State the blood parasite species.
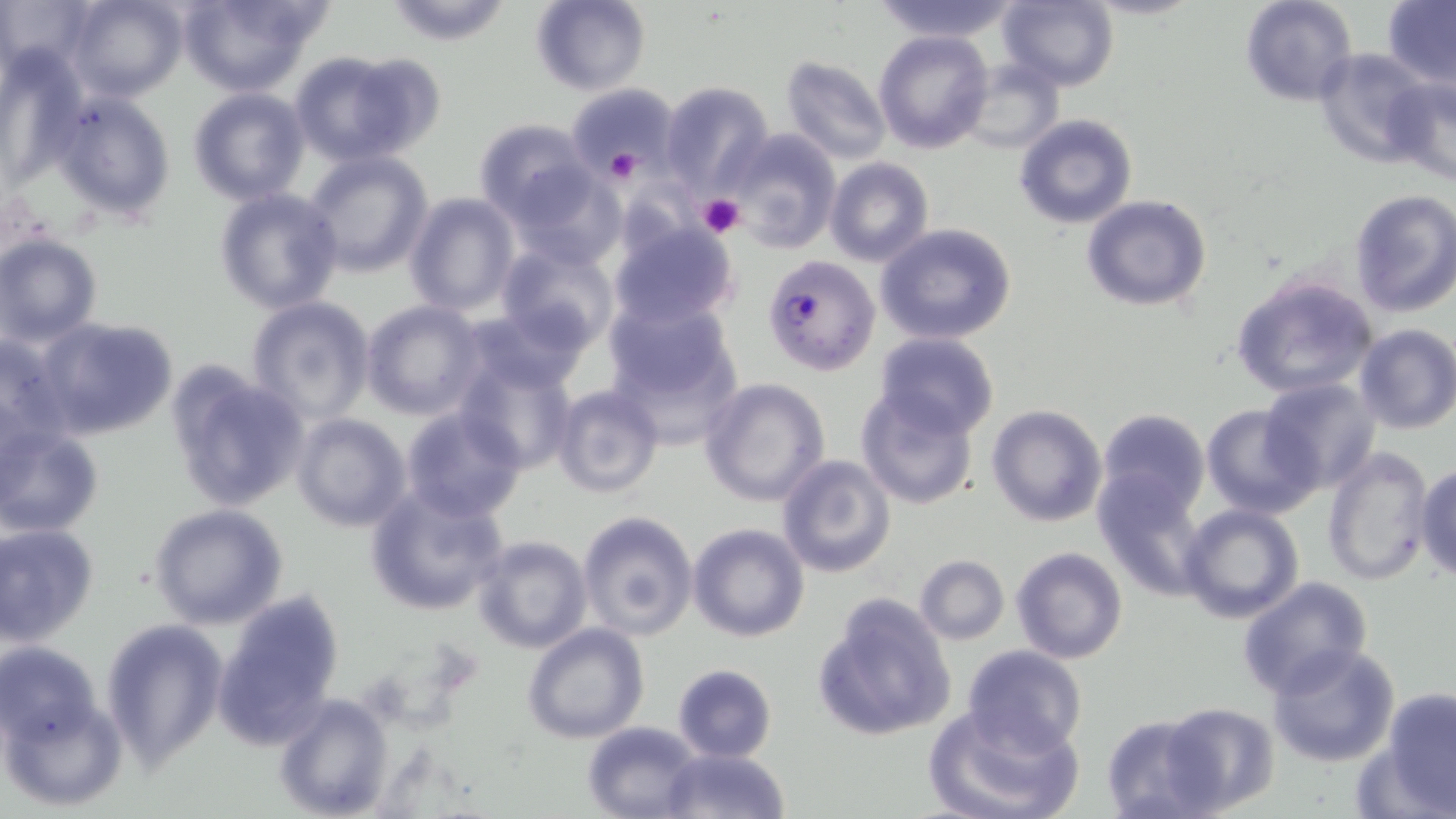
Plasmodium falciparum.

modality = optical microscopy
platelet locations = approximate bounding boxes as [x1, y1, x2, y2] in pixels: [606, 149, 642, 183], [697, 193, 747, 238]
image size = 1456×819 pixels
uninfected red blood cell locations = approximate bounding boxes as [x1, y1, x2, y2] in pixels: [0, 0, 93, 82], [65, 0, 188, 102], [383, 0, 516, 46], [870, 0, 1021, 42], [998, 0, 1119, 91], [1239, 0, 1358, 106], [531, 1, 652, 95], [1380, 1, 1456, 86], [172, 2, 328, 93], [874, 30, 994, 154], [1314, 47, 1435, 166], [287, 51, 428, 164], [778, 55, 892, 165], [959, 60, 1062, 154], [1383, 74, 1456, 188], [565, 82, 682, 178], [661, 82, 775, 198], [187, 87, 310, 205], [52, 91, 176, 223], [1014, 114, 1138, 230], [474, 120, 594, 225], [723, 128, 840, 253], [303, 149, 434, 278], [825, 159, 933, 267], [510, 164, 626, 267], [214, 188, 344, 314], [1349, 189, 1456, 317], [403, 191, 520, 316], [1083, 195, 1211, 311], [607, 218, 741, 331], [874, 222, 1017, 345], [0, 233, 102, 346], [496, 242, 618, 351], [1230, 272, 1380, 399], [601, 294, 742, 432], [246, 296, 376, 422], [360, 301, 486, 420], [462, 304, 593, 399], [37, 317, 180, 442], [1354, 324, 1456, 434], [0, 330, 76, 456], [874, 331, 1000, 440], [455, 353, 579, 474], [165, 363, 309, 512], [699, 377, 829, 507], [1261, 377, 1380, 493], [551, 383, 665, 499], [854, 383, 981, 511], [1201, 403, 1319, 519], [987, 405, 1108, 528], [399, 406, 528, 523], [1095, 408, 1210, 518], [291, 414, 412, 532], [1, 424, 103, 537], [1321, 444, 1434, 586], [775, 452, 897, 578], [1414, 463, 1456, 584], [1092, 471, 1209, 598], [365, 485, 508, 617], [149, 504, 290, 631], [1179, 505, 1305, 625], [577, 510, 698, 640], [0, 522, 100, 646], [688, 523, 811, 642], [472, 535, 593, 653], [1010, 547, 1128, 663], [914, 555, 1009, 645], [1237, 577, 1373, 701], [212, 590, 345, 749], [812, 595, 956, 742], [101, 617, 229, 769], [521, 622, 650, 744], [0, 639, 106, 752], [1267, 643, 1401, 768], [962, 645, 1088, 756], [671, 663, 778, 763], [1379, 687, 1456, 815], [0, 690, 124, 812], [273, 691, 395, 819], [1161, 701, 1279, 815], [925, 703, 1085, 819], [1100, 713, 1217, 817], [582, 719, 704, 819], [657, 748, 789, 819]
stain = May-Grünwald-Giemsa
magnification = 1000x
field of view = one of a larger specimen
Plasmodium falciparum-infected red blood cell locations = approximate bounding boxes as [x1, y1, x2, y2] in pixels: [762, 254, 880, 376]
preparation = thin blood film